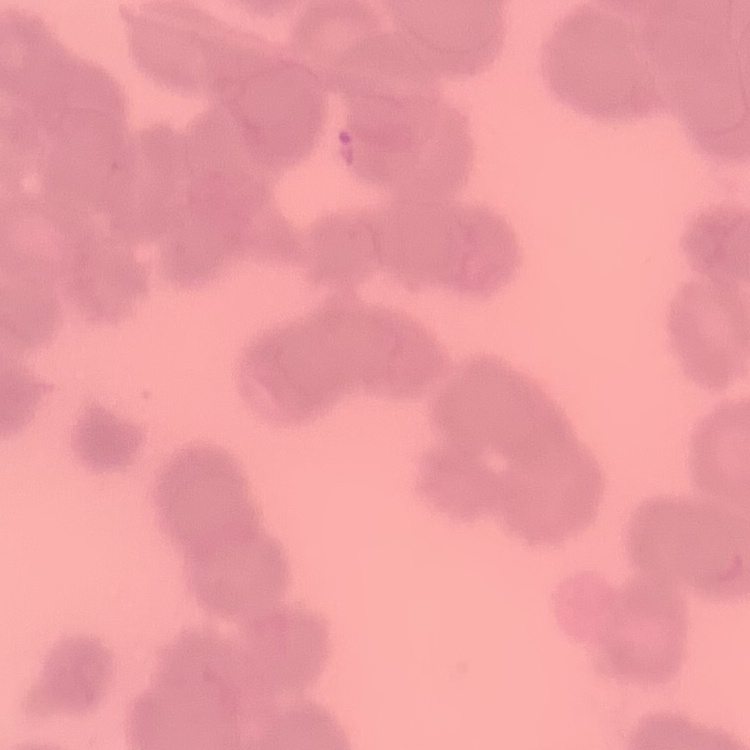 The erythrocytes show rouleaux formation. Thin blood film. Field's or Giemsa stain. Square crop of a larger photomicrograph.